Classify this cell by malaria status.
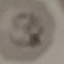
It is parasitized.

preparation = thin blood smear
stain = Giemsa
capture = smartphone through the microscope eyepiece
image type = cell patch, automatically extracted from a larger field of view and resized to 64 × 64 pixels